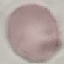
result: negative for malaria parasites
capture: smartphone camera at the microscope eyepiece
image_type: cell patch, automatically extracted from a larger field of view and resized to 64 × 64 pixels
stain: Giemsa
preparation: thin blood smear